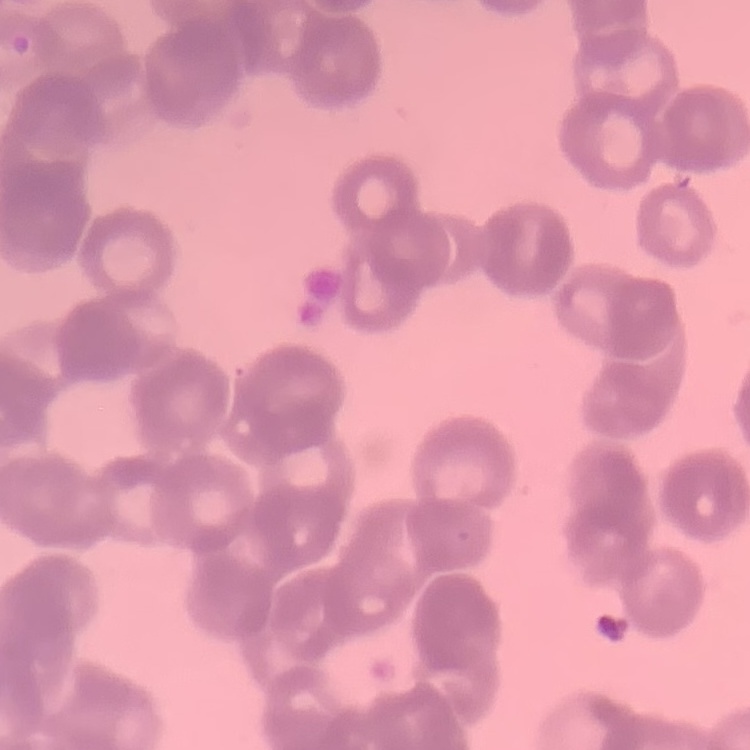

erythrocyte_morphology: rouleaux formation
image_type: one tile cut from a larger photomicrograph
stain: Field's or Giemsa
preparation: thin blood film